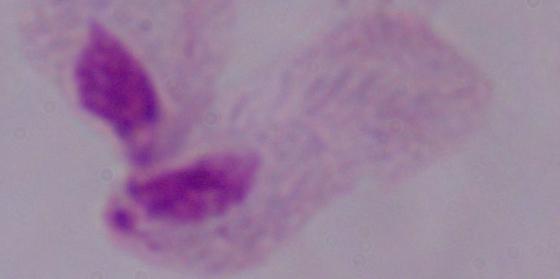

Summary:
  - Identification: trichomonad
  - Magnification: 1000x
  - Modality: micrograph